Classify this cell by malaria status.
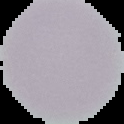
It is uninfected.

From a thin blood smear. Image is 124×124 pixels. The area outside the segmented cell region is set to black.